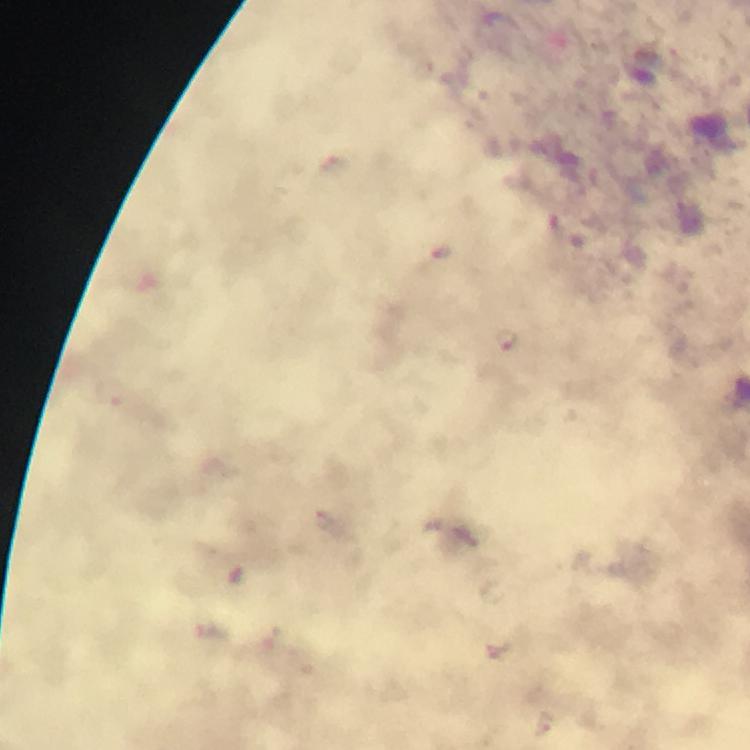

Approximate centers as {x, y} in pixels.
Summary:
  - Malaria parasite locations: {507, 339}
  - Context: from a diagnostic examination for malaria
  - Image size: 750×750 pixels
  - Capture: smartphone camera through the microscope
  - Cropped from: one field of view
  - Immersion oil: applied
  - Preparation: thick blood smear
  - Stain: Giemsa
  - Magnification: 100x